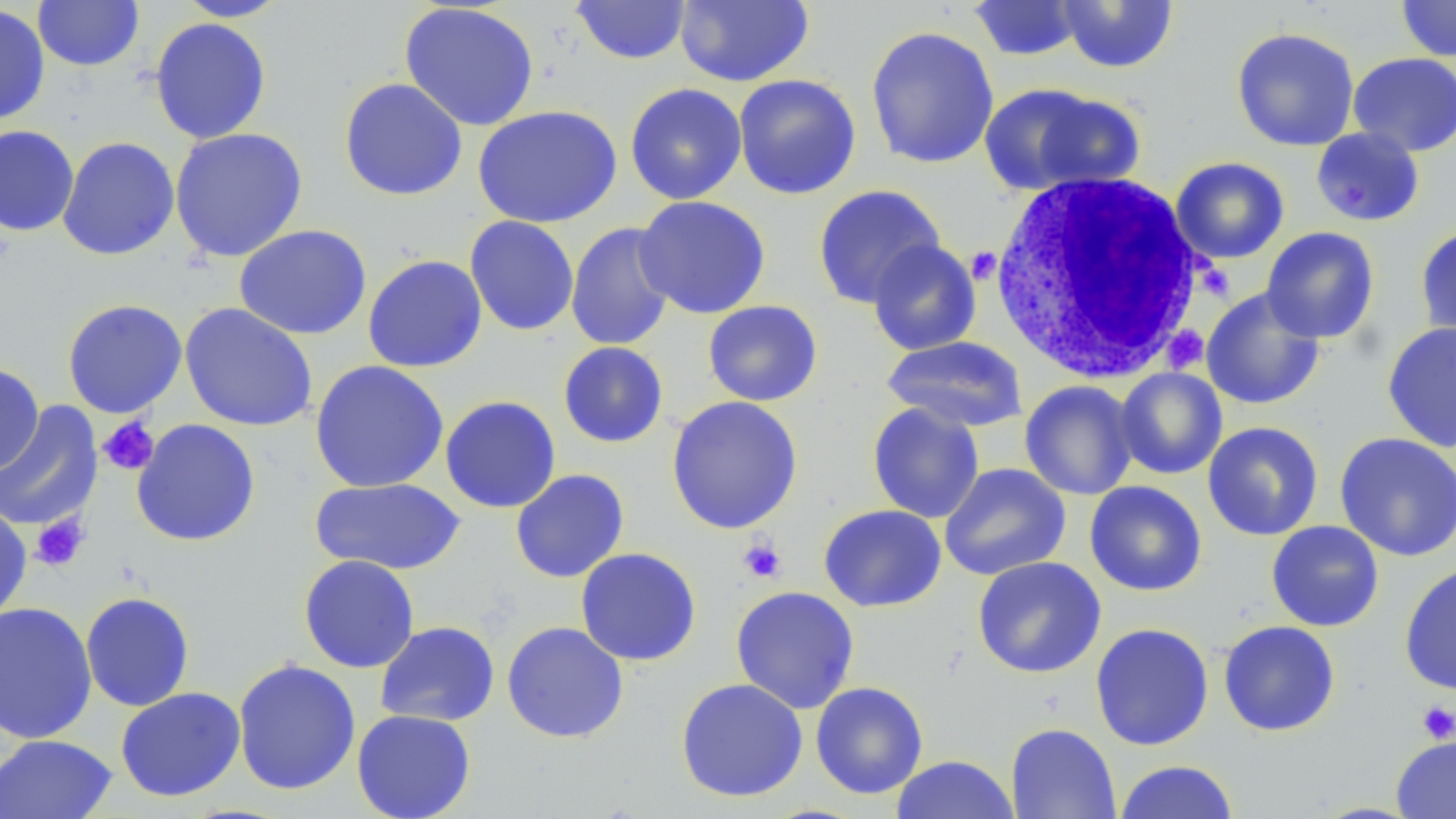

slide-level diagnosis = no evidence of blood parasites
platelet locations = approximate bounding boxes as (x1,y1)-(x2,y2) corner pairs in pixels: (97,417)-(159,476), (31,514)-(90,571), (738,538)-(786,583), (1418,701)-(1456,743)
preparation = thin blood film
image size = 1456×819 pixels
field of view = one of a larger specimen
stain = May-Grünwald-Giemsa
white blood cell locations = approximate bounding boxes as (x1,y1)-(x2,y2) corner pairs in pixels: (988,170)-(1210,384)
modality = light microscopy
uninfected red blood cell locations = approximate bounding boxes as (x1,y1)-(x2,y2) corner pairs in pixels: (32,0)-(144,72), (174,0)-(290,22), (674,0)-(814,87), (1396,0)-(1456,62), (570,1)-(692,65), (968,1)-(1084,61), (1056,1)-(1179,73), (398,2)-(540,132), (0,4)-(51,126), (149,16)-(272,145), (865,25)-(1000,169), (1231,26)-(1360,152), (1348,52)-(1456,157), (733,74)-(862,200), (339,77)-(468,201), (624,82)-(747,205), (978,82)-(1141,196), (473,105)-(622,228), (0,124)-(79,236), (1310,126)-(1425,227), (169,127)-(308,262), (57,136)-(180,261), (1170,156)-(1290,264), (813,184)-(946,309), (633,195)-(772,319), (464,215)-(579,336), (565,222)-(678,351), (234,224)-(372,340), (1415,224)-(1456,344), (1261,227)-(1380,343), (867,240)-(982,356), (362,254)-(487,373), (1201,288)-(1325,410), (61,299)-(188,418), (702,300)-(823,406), (179,303)-(318,432), (1382,321)-(1456,453), (881,335)-(1028,432), (557,341)-(669,448), (310,360)-(449,493), (0,362)-(45,476), (1115,367)-(1227,480), (1019,380)-(1139,500), (439,395)-(561,514), (666,395)-(804,535), (0,401)-(103,532), (867,402)-(985,523), (131,419)-(261,547), (1202,421)-(1324,541), (1335,432)-(1456,562), (939,462)-(1071,581), (510,468)-(629,583), (309,477)-(466,575), (1085,480)-(1207,596), (0,502)-(32,624), (818,504)-(947,612), (1266,520)-(1384,632), (575,547)-(702,666), (298,554)-(420,673), (972,556)-(1106,678), (1399,562)-(1456,695), (730,585)-(860,714), (80,591)-(195,711), (0,600)-(98,744), (1218,620)-(1341,737), (374,621)-(500,727), (501,621)-(629,744), (1090,622)-(1214,750), (232,658)-(361,796), (675,677)-(809,802), (810,681)-(928,799), (115,687)-(246,802), (351,708)-(476,819), (1005,722)-(1121,819), (0,734)-(118,819), (1391,735)-(1456,818), (890,755)-(1020,818), (1113,760)-(1238,819)
magnification = 1000x